Classify the preparation.
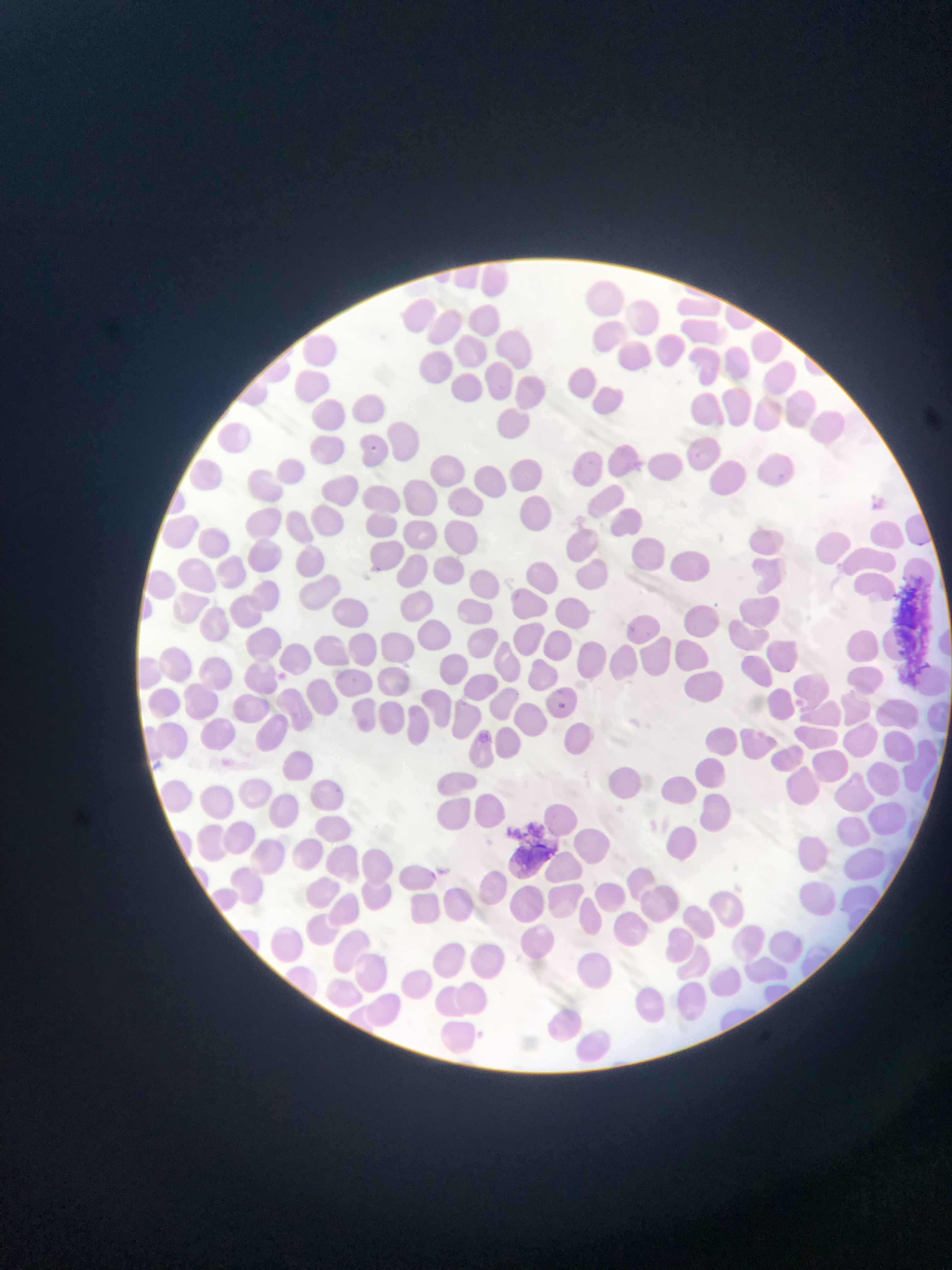

Thin blood film.

{
  "country": "Ghana",
  "artifact_stain_precipitate_or_debris_locations": "approximate bounding boxes as [left, top, right, bottom] in pixels: [901, 575, 937, 681], [508, 825, 555, 869]",
  "image_size": "952×1270 pixels",
  "capture": "mobile-phone photograph through a microscope",
  "field_of_view": "single"
}